Assess this cell for malaria.
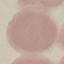

Uninfected.

Summary:
  - Image type: automatically extracted cell patch, resized to 64 × 64 pixels
  - Preparation: thin blood film
  - Capture: smartphone camera at the microscope eyepiece
  - Stain: Giemsa